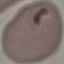

Result: malaria parasites identified. Photographed with a smartphone camera at the microscope eyepiece. Giemsa stain. Cell patch, automatically extracted from a larger field of view and resized to 64 × 64 pixels. Thin smear of blood.